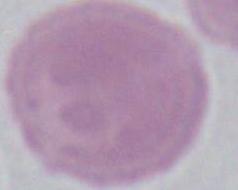

{
  "magnification": "1000x",
  "identification": "red blood cell",
  "modality": "photomicrograph"
}